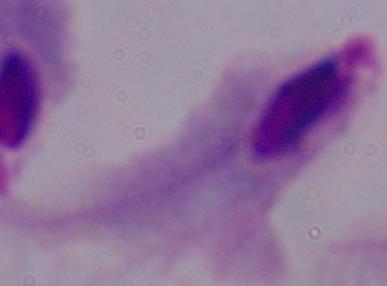

magnification: 1000x
identification: trichomonad
modality: photomicrograph